Report the malaria status.
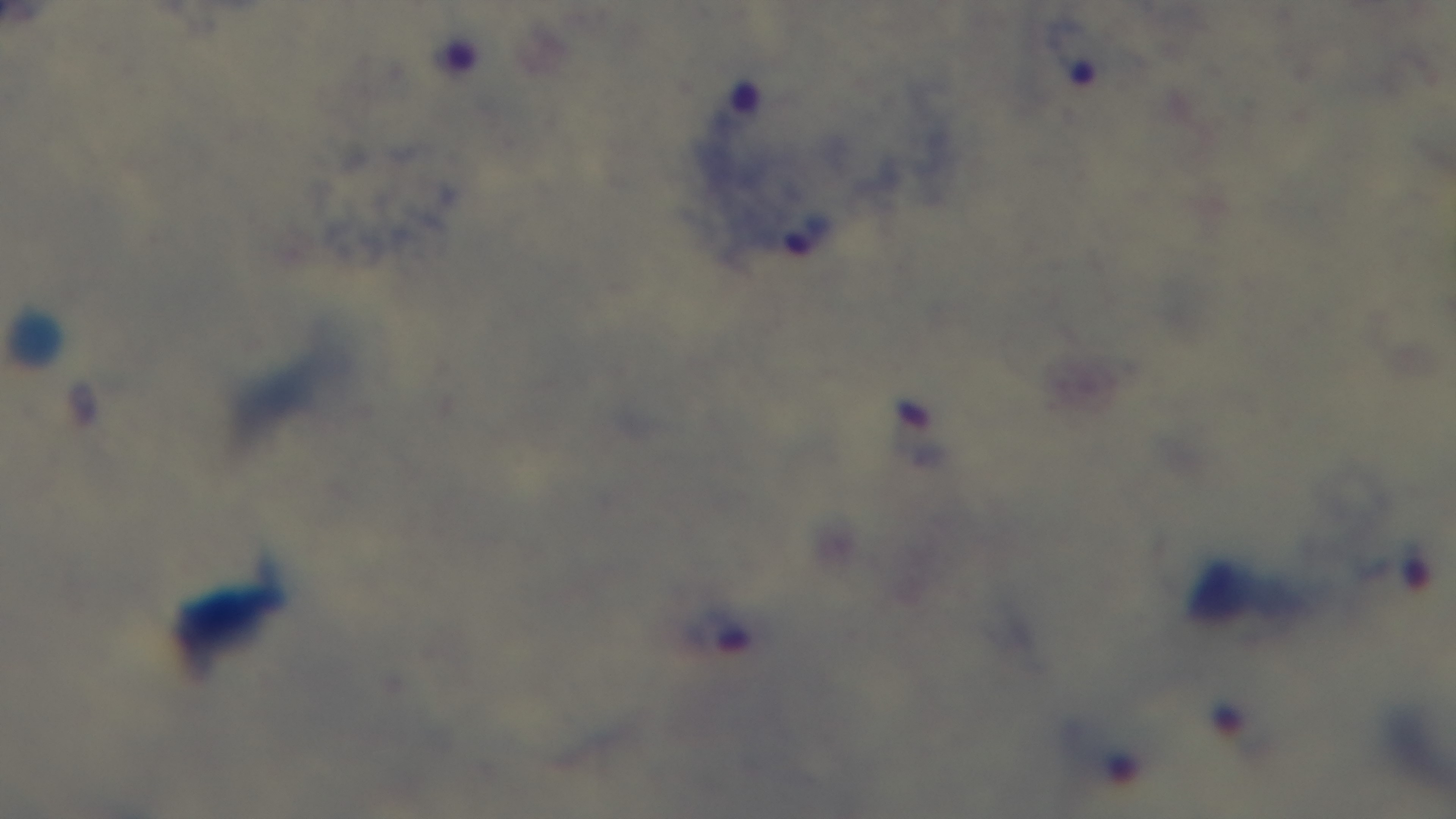

Infected.

field_of_view: one from the slide
modality: light microscopy
objective: 100x oil immersion
preparation: thick blood film
stain: Giemsa
capture: mounted 4K digital camera